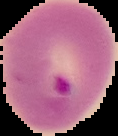

image size = 118×136 pixels
preparation = thin blood film
malaria status = parasitized
image type = segmented cell region on a black background